Describe the morphology of the red blood cells.
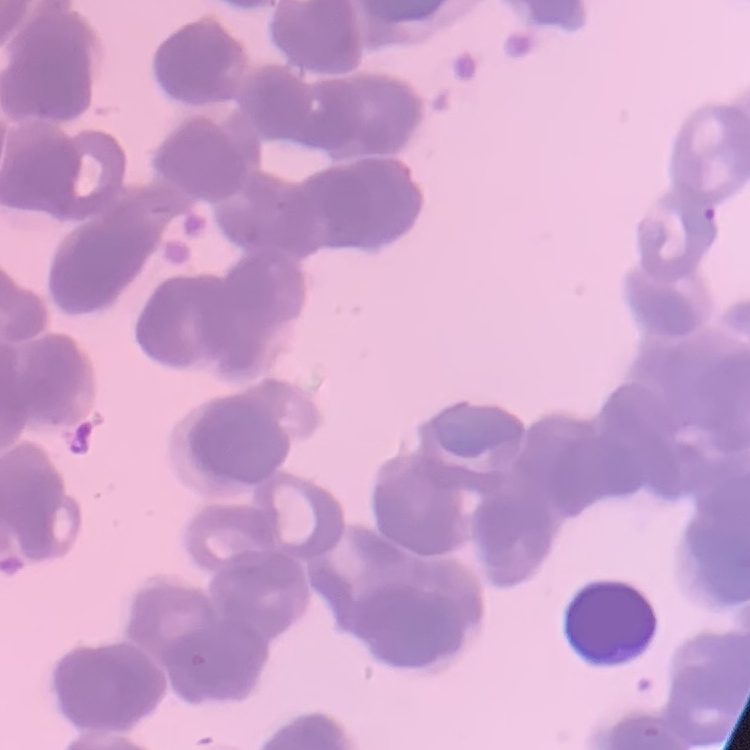
Rouleaux formation.

Summary:
  - Preparation: thin blood smear
  - Image type: square crop of a larger photomicrograph
  - Stain: Field's or Giemsa